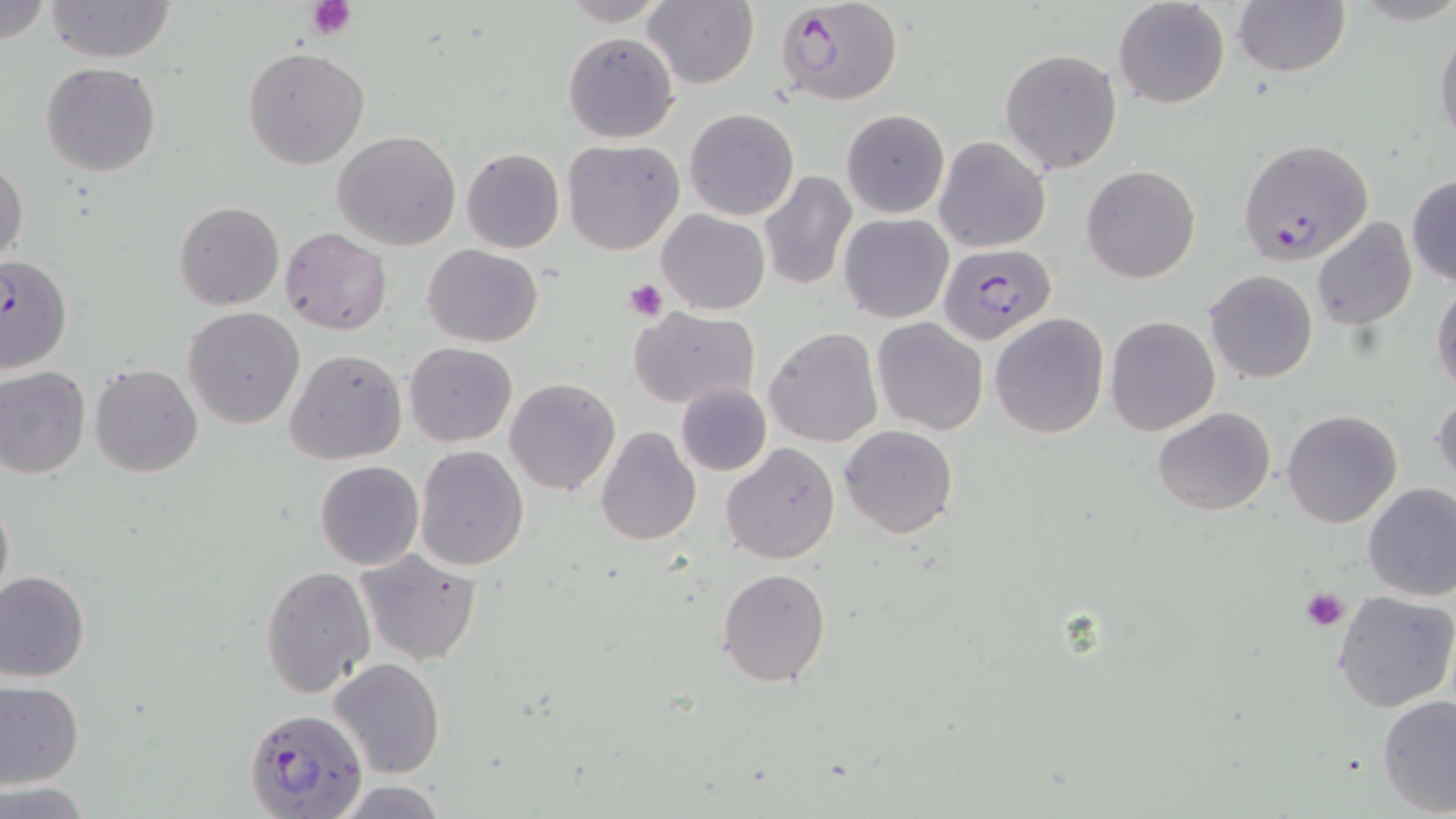

Approximate bounding boxes as named x1/y1/x2/y2 corners in pixels. Uninfected red blood cell locations: (x1=42, y1=0, x2=179, y2=64), (x1=552, y1=0, x2=677, y2=26), (x1=643, y1=0, x2=760, y2=89), (x1=1113, y1=0, x2=1230, y2=109), (x1=1232, y1=0, x2=1350, y2=77), (x1=0, y1=1, x2=53, y2=47), (x1=1434, y1=27, x2=1456, y2=151), (x1=563, y1=31, x2=679, y2=143), (x1=243, y1=47, x2=368, y2=170), (x1=999, y1=48, x2=1124, y2=173), (x1=41, y1=62, x2=163, y2=177), (x1=684, y1=108, x2=798, y2=220), (x1=841, y1=109, x2=950, y2=219), (x1=332, y1=130, x2=462, y2=251), (x1=934, y1=136, x2=1050, y2=253), (x1=563, y1=138, x2=684, y2=255), (x1=461, y1=148, x2=564, y2=254), (x1=1, y1=156, x2=27, y2=268), (x1=1081, y1=164, x2=1200, y2=283), (x1=759, y1=172, x2=856, y2=291), (x1=1406, y1=175, x2=1456, y2=287), (x1=174, y1=201, x2=284, y2=310), (x1=656, y1=211, x2=769, y2=315), (x1=838, y1=213, x2=954, y2=323), (x1=1311, y1=217, x2=1419, y2=331), (x1=280, y1=228, x2=391, y2=336), (x1=422, y1=245, x2=543, y2=347), (x1=0, y1=255, x2=72, y2=375), (x1=1203, y1=270, x2=1318, y2=384), (x1=1432, y1=280, x2=1456, y2=398), (x1=627, y1=305, x2=761, y2=410), (x1=182, y1=307, x2=306, y2=428), (x1=990, y1=314, x2=1109, y2=439), (x1=1104, y1=315, x2=1220, y2=436), (x1=871, y1=318, x2=988, y2=435), (x1=765, y1=328, x2=883, y2=447), (x1=405, y1=342, x2=517, y2=446), (x1=284, y1=349, x2=407, y2=465), (x1=89, y1=364, x2=202, y2=478), (x1=0, y1=366, x2=91, y2=479), (x1=504, y1=378, x2=619, y2=496), (x1=675, y1=383, x2=771, y2=476), (x1=1432, y1=388, x2=1456, y2=490), (x1=1152, y1=408, x2=1276, y2=515), (x1=1282, y1=410, x2=1403, y2=528), (x1=840, y1=425, x2=957, y2=539), (x1=595, y1=428, x2=701, y2=548), (x1=721, y1=442, x2=840, y2=564), (x1=414, y1=444, x2=529, y2=571), (x1=315, y1=461, x2=424, y2=570), (x1=1361, y1=484, x2=1456, y2=602), (x1=0, y1=489, x2=13, y2=609), (x1=353, y1=547, x2=481, y2=668), (x1=260, y1=565, x2=374, y2=697), (x1=716, y1=566, x2=832, y2=687), (x1=0, y1=569, x2=89, y2=682), (x1=1332, y1=591, x2=1456, y2=713), (x1=330, y1=657, x2=445, y2=779), (x1=0, y1=682, x2=84, y2=787), (x1=1377, y1=694, x2=1456, y2=817), (x1=332, y1=780, x2=453, y2=817), (x1=1, y1=782, x2=92, y2=816). Platelet locations: (x1=305, y1=0, x2=357, y2=38), (x1=624, y1=278, x2=667, y2=321), (x1=1301, y1=587, x2=1350, y2=631). Plasmodium falciparum-infected red blood cell locations: (x1=775, y1=0, x2=904, y2=106), (x1=1237, y1=138, x2=1373, y2=263), (x1=938, y1=242, x2=1054, y2=344), (x1=245, y1=708, x2=367, y2=818). Slide-level diagnosis: Plasmodium falciparum. Thin blood film. Captured at 1000x magnification. May-Grünwald-Giemsa-stained preparation. Image is 1456×819 pixels. Single field of view. Optical microscopy.